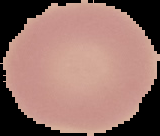 Image is 160×136 pixels. Malaria status: uninfected. From a thin blood film. The area outside the segmented cell region is set to black.